Report the malaria status.
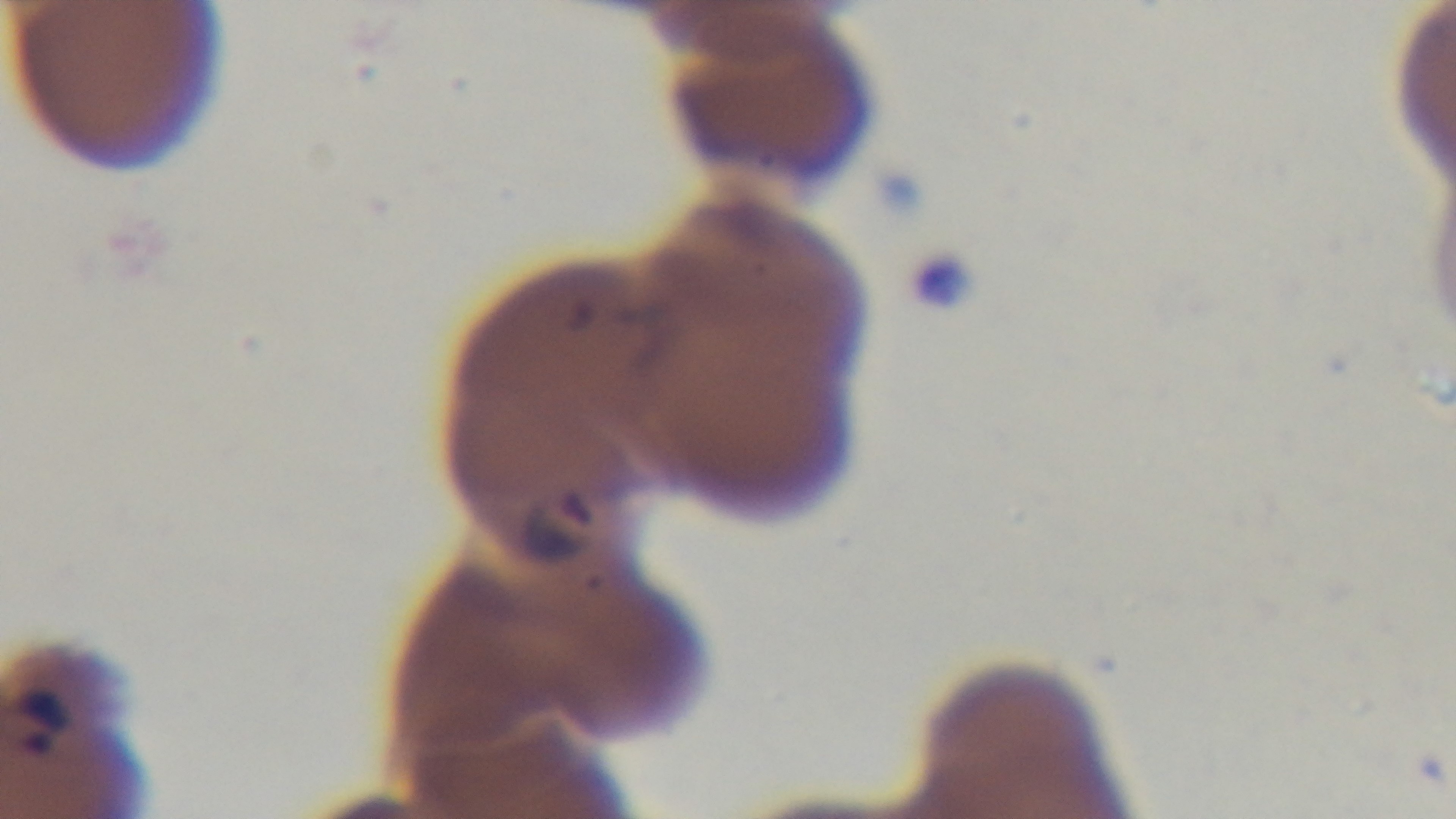
Positive.

objective: 100x oil immersion
preparation: thin smear
field_of_view: single
stain: Giemsa
modality: light microscopy
capture: mounted 4K digital camera